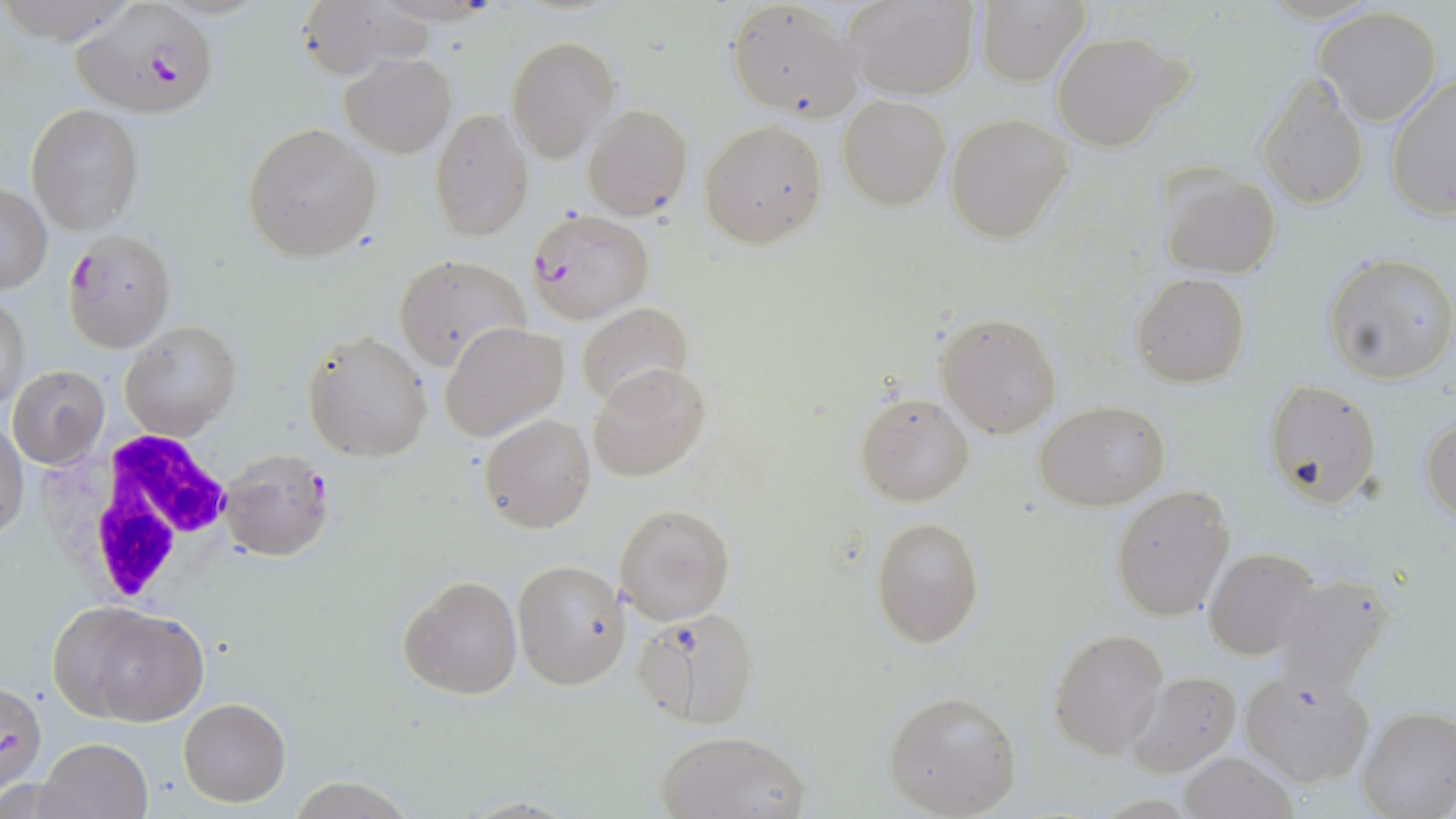
Summary:
  - Coordinate format: approximate bounding boxes as named x1/y1/x2/y2 corners in pixels
  - Plasmodium falciparum-infected red blood cell locations: (x1=72, y1=2, x2=218, y2=117), (x1=525, y1=208, x2=656, y2=324), (x1=65, y1=230, x2=174, y2=351), (x1=217, y1=448, x2=334, y2=560)
  - Uninfected red blood cell locations: (x1=725, y1=0, x2=862, y2=122), (x1=846, y1=0, x2=978, y2=98), (x1=977, y1=1, x2=1089, y2=85), (x1=291, y1=2, x2=428, y2=79), (x1=1312, y1=7, x2=1444, y2=127), (x1=1049, y1=32, x2=1189, y2=152), (x1=507, y1=37, x2=619, y2=161), (x1=340, y1=54, x2=455, y2=159), (x1=1256, y1=75, x2=1369, y2=210), (x1=1385, y1=75, x2=1456, y2=220), (x1=838, y1=95, x2=950, y2=210), (x1=583, y1=103, x2=694, y2=220), (x1=28, y1=104, x2=144, y2=235), (x1=429, y1=108, x2=533, y2=240), (x1=945, y1=113, x2=1071, y2=242), (x1=700, y1=118, x2=827, y2=249), (x1=243, y1=123, x2=380, y2=261), (x1=1161, y1=172, x2=1280, y2=279), (x1=0, y1=184, x2=51, y2=293), (x1=1323, y1=252, x2=1456, y2=384), (x1=393, y1=253, x2=529, y2=371), (x1=1131, y1=273, x2=1251, y2=388), (x1=1, y1=291, x2=28, y2=411), (x1=576, y1=302, x2=694, y2=409), (x1=936, y1=312, x2=1060, y2=437), (x1=119, y1=320, x2=239, y2=442), (x1=440, y1=321, x2=568, y2=442), (x1=302, y1=328, x2=433, y2=463), (x1=7, y1=364, x2=109, y2=469), (x1=587, y1=364, x2=710, y2=481), (x1=1261, y1=380, x2=1380, y2=508), (x1=855, y1=391, x2=975, y2=506), (x1=1036, y1=400, x2=1169, y2=511), (x1=479, y1=413, x2=595, y2=532), (x1=0, y1=414, x2=27, y2=544), (x1=1422, y1=414, x2=1455, y2=523), (x1=1110, y1=485, x2=1235, y2=620), (x1=616, y1=502, x2=736, y2=625), (x1=870, y1=516, x2=984, y2=649), (x1=1202, y1=550, x2=1319, y2=661), (x1=515, y1=559, x2=631, y2=688), (x1=397, y1=573, x2=523, y2=700), (x1=1271, y1=575, x2=1397, y2=695), (x1=53, y1=603, x2=208, y2=726), (x1=634, y1=606, x2=759, y2=729), (x1=1048, y1=627, x2=1169, y2=759), (x1=1239, y1=668, x2=1375, y2=787), (x1=1125, y1=670, x2=1240, y2=777), (x1=1, y1=683, x2=47, y2=793), (x1=882, y1=690, x2=1023, y2=817), (x1=178, y1=697, x2=290, y2=806), (x1=1356, y1=706, x2=1455, y2=819), (x1=656, y1=728, x2=810, y2=819), (x1=37, y1=737, x2=150, y2=819), (x1=1178, y1=750, x2=1301, y2=819)
  - White blood cell locations: (x1=45, y1=430, x2=243, y2=609)
  - Slide-level diagnosis: Plasmodium falciparum
  - Field of view: single
  - Preparation: thin blood film
  - Image size: 1456×819 pixels
  - Stain: May-Grünwald-Giemsa
  - Modality: light microscopy
  - Magnification: 1000x